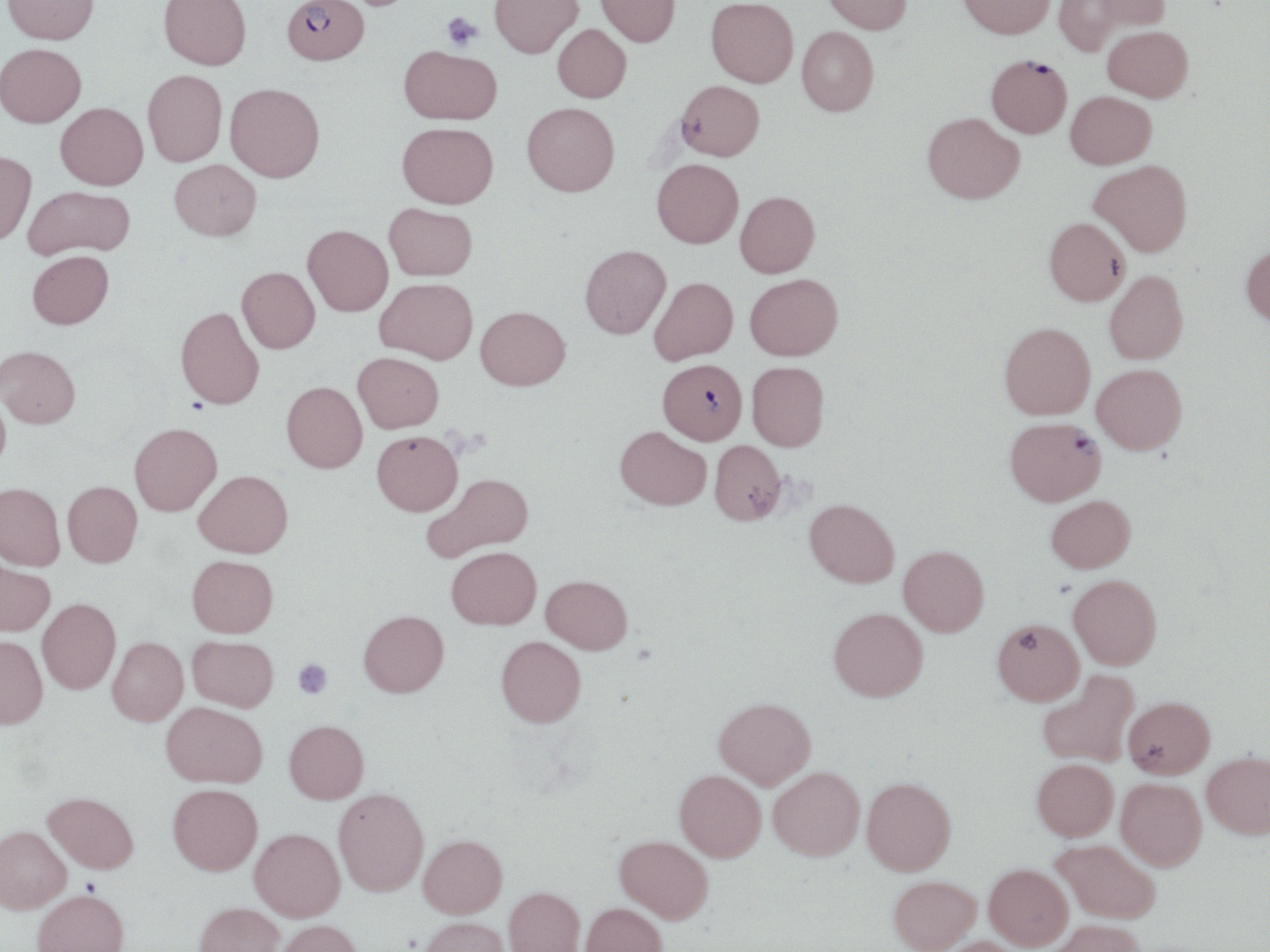

Summary:
  - Coordinate format: approximate bounding boxes as (x1, y1, x2, y2) in pixels
  - Platelet locations: (441, 12, 483, 51), (292, 658, 332, 699)
  - Uninfected red blood cell locations: (2, 0, 99, 45), (158, 0, 251, 71), (489, 0, 582, 58), (596, 0, 679, 47), (705, 0, 798, 87), (823, 0, 912, 34), (957, 0, 1055, 39), (1087, 0, 1169, 33), (1054, 1, 1129, 55), (553, 24, 631, 103), (1103, 25, 1193, 101), (797, 26, 878, 115), (0, 44, 86, 129), (399, 46, 501, 125), (143, 70, 226, 167), (676, 80, 764, 161), (226, 83, 324, 183), (1066, 91, 1156, 168), (522, 101, 619, 195), (55, 103, 148, 190), (923, 112, 1024, 203), (397, 122, 498, 208), (0, 151, 36, 246), (652, 158, 743, 247), (170, 159, 261, 240), (1089, 160, 1192, 255), (23, 185, 135, 259), (735, 191, 819, 277), (384, 202, 477, 280), (1044, 217, 1130, 305), (302, 225, 393, 316), (580, 244, 670, 339), (1241, 244, 1270, 327), (28, 250, 114, 329), (237, 266, 319, 353), (1105, 270, 1188, 364), (745, 273, 842, 360), (648, 277, 737, 363), (375, 278, 478, 364), (176, 305, 265, 409), (476, 306, 570, 390), (1000, 322, 1095, 418), (0, 345, 80, 428), (353, 352, 443, 432), (747, 361, 829, 451), (1092, 364, 1187, 453), (281, 381, 367, 473), (0, 388, 12, 474), (129, 423, 221, 515), (615, 426, 711, 510), (372, 430, 463, 515), (710, 440, 786, 525), (194, 470, 293, 557), (422, 472, 533, 562), (62, 481, 142, 567), (0, 482, 65, 570), (1046, 495, 1135, 572), (805, 499, 899, 587), (899, 545, 989, 635), (447, 546, 541, 629), (187, 555, 278, 637), (0, 558, 54, 635), (541, 575, 632, 653), (1069, 575, 1162, 669), (37, 598, 121, 694), (829, 607, 928, 701), (358, 610, 449, 697), (992, 618, 1084, 704), (0, 635, 48, 729), (188, 635, 278, 711), (496, 636, 586, 727), (107, 637, 187, 725), (1038, 670, 1139, 767), (1124, 696, 1215, 778), (714, 697, 816, 788), (161, 701, 267, 787), (285, 720, 369, 803), (1202, 752, 1270, 838), (1032, 758, 1119, 840), (769, 766, 864, 860), (675, 769, 766, 861), (862, 777, 956, 875), (1117, 778, 1206, 870), (168, 784, 262, 875), (333, 787, 429, 896), (44, 791, 139, 873), (0, 826, 71, 912), (250, 828, 345, 920), (419, 834, 507, 918), (615, 835, 713, 922), (1052, 839, 1160, 923), (984, 864, 1072, 949), (889, 875, 980, 951), (504, 886, 584, 952), (33, 889, 129, 952), (194, 902, 284, 952), (581, 902, 667, 952), (419, 916, 508, 952), (276, 919, 364, 952), (1049, 919, 1144, 952), (934, 936, 1025, 952)
  - Plasmodium falciparum-infected red blood cell locations: (282, 0, 369, 65), (986, 54, 1072, 138), (658, 359, 747, 444), (1005, 417, 1105, 505)
  - Slide-level diagnosis: Plasmodium falciparum
  - Preparation: thin blood smear
  - Stain: May-Grünwald-Giemsa
  - Image size: 1270×952 pixels
  - Field of view: one of a larger specimen
  - Modality: optical microscopy
  - Magnification: 1000x